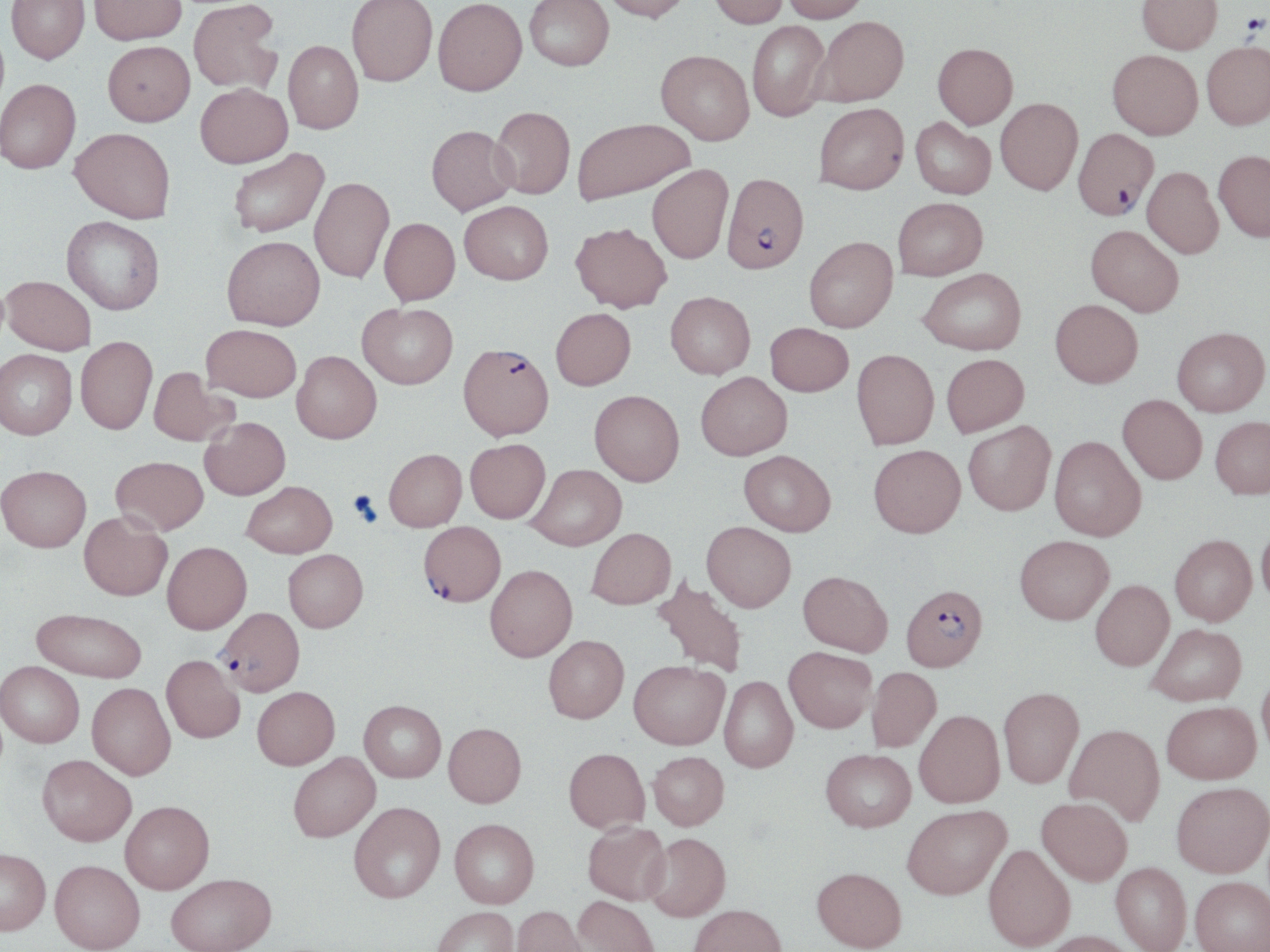

slide-level diagnosis = Plasmodium falciparum
preparation = thin blood film
platelet locations = approximate bounding boxes as (x1,y1)-(x2,y2) corner pairs in pixels: (1240,14)-(1268,36), (348,490)-(382,525)
modality = light microscopy
image size = 1270×952 pixels
Plasmodium falciparum-infected red blood cell locations = approximate bounding boxes as (x1,y1)-(x2,y2) corner pairs in pixels: (1074,129)-(1158,221), (722,172)-(809,275), (458,344)-(554,439), (418,521)-(505,607), (901,583)-(988,671), (216,607)-(304,695)
field of view = one of a larger specimen
stain = May-Grünwald-Giemsa
magnification = 1000x
uninfected red blood cell locations = approximate bounding boxes as (x1,y1)-(x2,y2) corner pairs in pixels: (6,0)-(89,64), (89,0)-(186,45), (188,0)-(283,94), (347,0)-(437,89), (525,0)-(614,73), (600,0)-(692,25), (708,0)-(788,31), (782,0)-(868,25), (1135,0)-(1222,56), (432,1)-(527,99), (814,18)-(909,108), (747,22)-(831,122), (103,40)-(195,126), (283,40)-(363,135), (1203,44)-(1270,132), (932,45)-(1018,132), (654,51)-(754,147), (1108,52)-(1202,142), (0,79)-(81,173), (195,83)-(293,168), (996,99)-(1083,198), (815,103)-(909,196), (490,107)-(574,200), (572,118)-(694,205), (911,119)-(996,200), (426,126)-(517,216), (70,127)-(175,223), (228,148)-(329,237), (1214,153)-(1270,244), (647,164)-(733,264), (1142,168)-(1223,260), (309,177)-(394,282), (893,198)-(988,280), (459,200)-(553,284), (62,216)-(164,315), (379,217)-(460,305), (571,222)-(672,312), (1086,224)-(1184,316), (222,235)-(325,330), (804,236)-(898,332), (919,268)-(1027,355), (2,275)-(96,354), (665,292)-(755,378), (1050,299)-(1143,387), (358,303)-(457,389), (550,307)-(636,389), (765,322)-(853,396), (201,324)-(301,401), (1172,327)-(1269,415), (76,336)-(157,434), (0,349)-(77,439), (851,349)-(938,449), (292,350)-(381,443), (941,354)-(1029,437), (149,367)-(236,446), (696,372)-(792,460), (589,390)-(684,486), (1117,394)-(1207,484), (1210,416)-(1270,498), (200,417)-(290,500), (963,420)-(1056,515), (1050,435)-(1146,541), (465,439)-(550,523), (869,444)-(966,537), (383,449)-(466,531), (739,450)-(835,535), (111,456)-(208,535), (526,464)-(626,550), (0,465)-(91,552), (242,481)-(337,557), (79,511)-(172,600), (1257,520)-(1270,610), (702,521)-(796,612), (586,527)-(676,609), (1169,534)-(1257,625), (1015,535)-(1114,624), (162,541)-(251,633), (283,549)-(368,632), (484,565)-(577,661), (797,570)-(893,656), (652,574)-(749,678), (1090,579)-(1174,670), (32,608)-(147,681), (1147,623)-(1246,705), (543,635)-(629,723), (784,646)-(877,732), (162,655)-(244,743), (629,659)-(729,749), (1,661)-(84,747), (867,667)-(942,752), (1257,668)-(1270,762), (719,676)-(798,772), (87,682)-(176,780), (252,686)-(339,769), (998,686)-(1084,788), (359,700)-(445,782), (1162,701)-(1260,783), (914,709)-(1004,808), (443,723)-(526,807), (1065,723)-(1165,825), (564,747)-(650,832), (821,748)-(916,832), (648,751)-(729,829), (288,752)-(380,842), (37,754)-(136,846), (1171,781)-(1270,877), (1036,797)-(1132,885), (120,800)-(214,893), (349,801)-(445,903), (902,804)-(1009,899), (450,818)-(539,908), (583,821)-(671,905), (643,832)-(730,921), (983,843)-(1075,951), (0,848)-(50,935), (50,860)-(145,952), (1111,862)-(1191,952), (812,866)-(906,952), (166,873)-(276,952), (1190,876)-(1270,952), (573,895)-(661,952), (689,903)-(787,952), (512,904)-(589,952), (432,907)-(519,952), (1040,930)-(1139,952)